Classify this cell by malaria status.
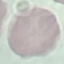

It is uninfected.

{
  "image_type": "automatically extracted cell patch, resized to 64 × 64 pixels",
  "capture": "smartphone camera at the microscope eyepiece",
  "stain": "Giemsa",
  "preparation": "thin blood smear"
}